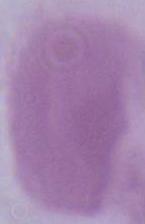

{
  "modality": "micrograph",
  "magnification": "1000x",
  "identification": "erythrocyte"
}